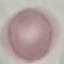

Summary:
  - Malaria status: uninfected
  - Preparation: thin blood film
  - Stain: Giemsa
  - Capture: smartphone through the microscope eyepiece
  - Image type: automatically extracted cell patch, resized to 64 × 64 pixels